Locate every Plasmodium parasite.
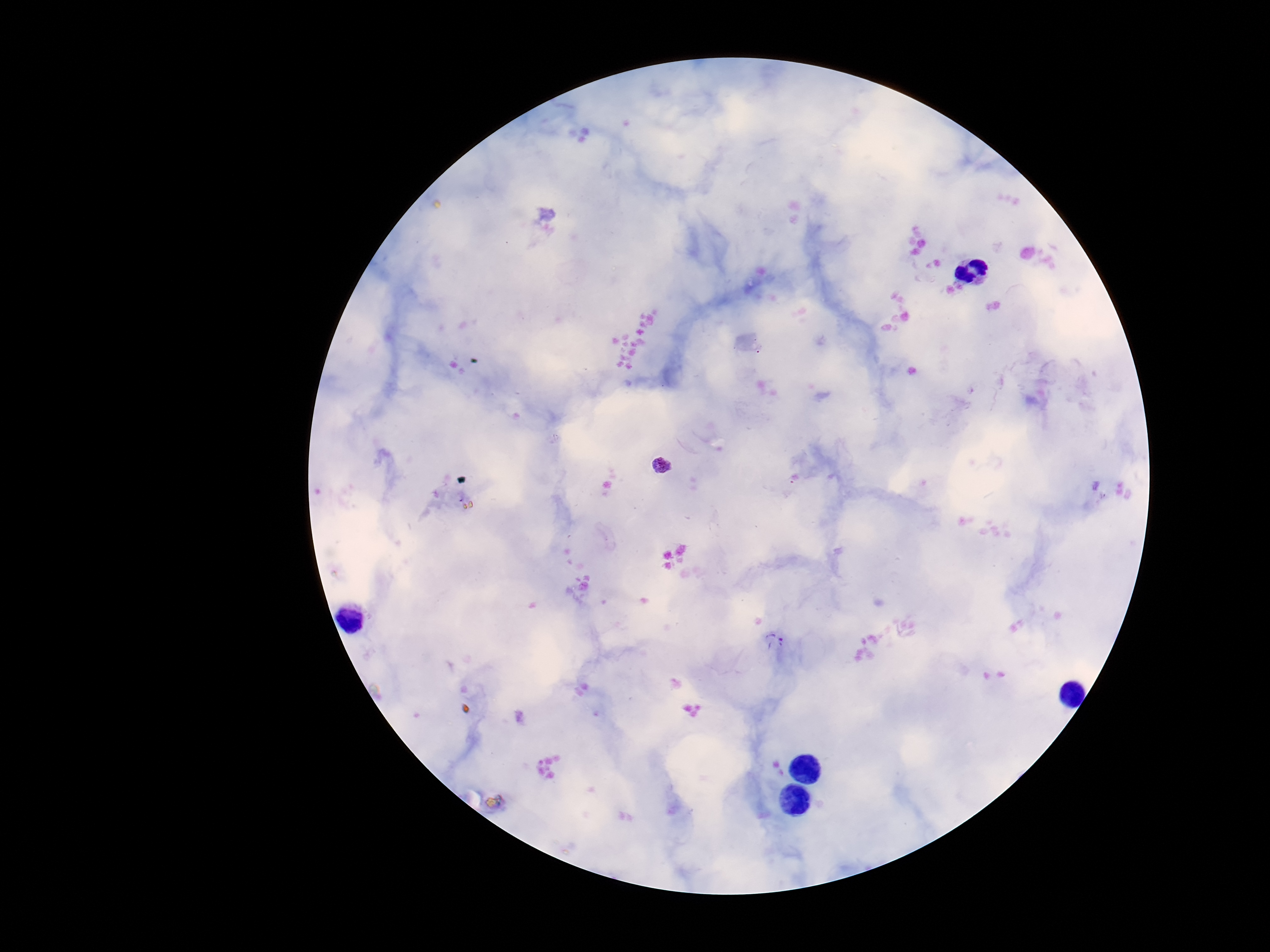

Approximate centers as {x, y} in pixels.
Plasmodium parasites: {662, 465}, {775, 642}.

patient malaria status = positive
field of view = one from this slide
preparation = thick blood smear
image size = 1270×952 pixels
magnification = 100x
capture = smartphone camera through the microscope eyepiece
stain = Giemsa